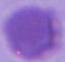
identification = erythrocyte
magnification = 1000x
modality = micrograph